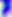 Photomicrograph. 400x magnification. Toxoplasma gondii is seen.